Classify this cell by malaria status.
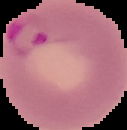
Parasitized.

From a thin blood smear. Segmented cell region on a black background. Image is 127×130 pixels.